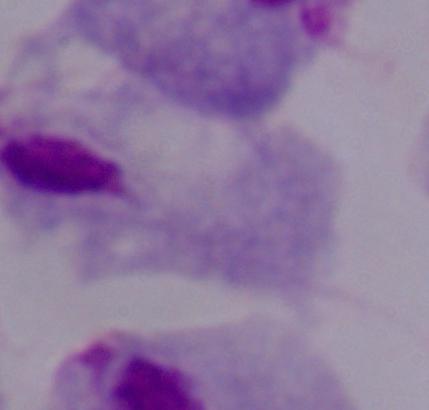

{
  "modality": "micrograph",
  "magnification": "1000x",
  "identification": "trichomonad"
}